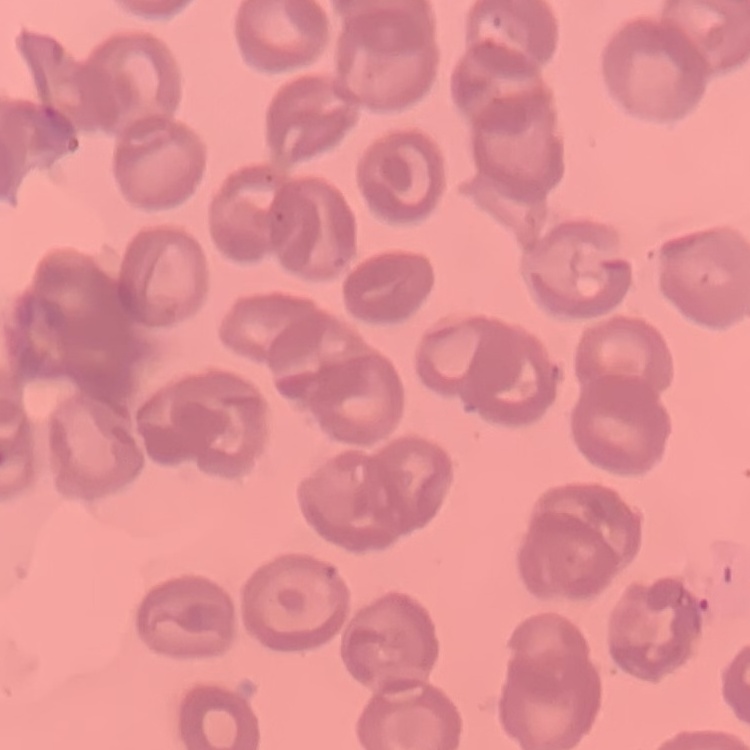
The erythrocytes show no rouleaux formation. One tile cut from a larger photomicrograph. Stained with either Field's or Giemsa. Thin peripheral smear.